Assess this cell for malaria.
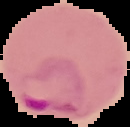
Parasitized.

Summary:
  - Image size: 130×127 pixels
  - Preparation: thin blood film
  - Image type: cell region segmented out of the field of view; surrounding area masked to black